Report the malaria status of this cell.
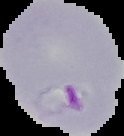
It is parasitized.

image size = 124×136 pixels
preparation = thin blood film
image type = cell region segmented out of the field of view; surrounding area masked to black